State which parasite is depicted.
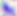
This is Toxoplasma gondii.

{
  "magnification": "400x",
  "modality": "photomicrograph"
}